Identify the parasite.
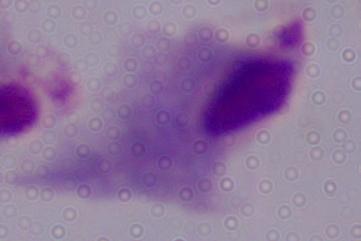

A trichomonad.

magnification = 1000x
modality = photomicrograph